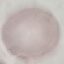

{
  "malaria_status": "uninfected",
  "preparation": "thin smear",
  "capture": "smartphone camera at the microscope eyepiece",
  "image_type": "cell patch, automatically extracted from a larger field of view and resized to 64 × 64 pixels",
  "stain": "Giemsa"
}